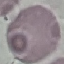

Summary:
  - Result: negative for malaria parasites
  - Capture: smartphone camera at the microscope eyepiece
  - Stain: Giemsa
  - Image type: automatically extracted cell patch, resized to 64 × 64 pixels
  - Preparation: thin blood smear